Assess this cell for malaria.
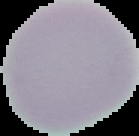
It is uninfected.

Summary:
  - Image type: cell region segmented out of the field of view; surrounding area masked to black
  - Preparation: thin blood smear
  - Image size: 139×136 pixels